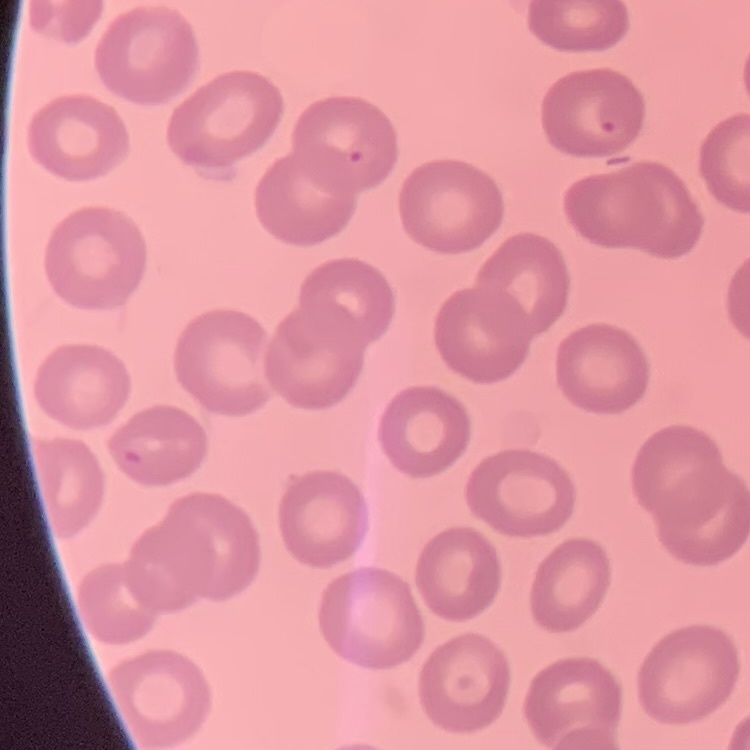
The red blood cells show no rouleaux formation. Square crop of a larger photomicrograph. Stained with either Field's or Giemsa. Thin blood film.